Give the position of every Plasmodium parasite and every leukocyte.
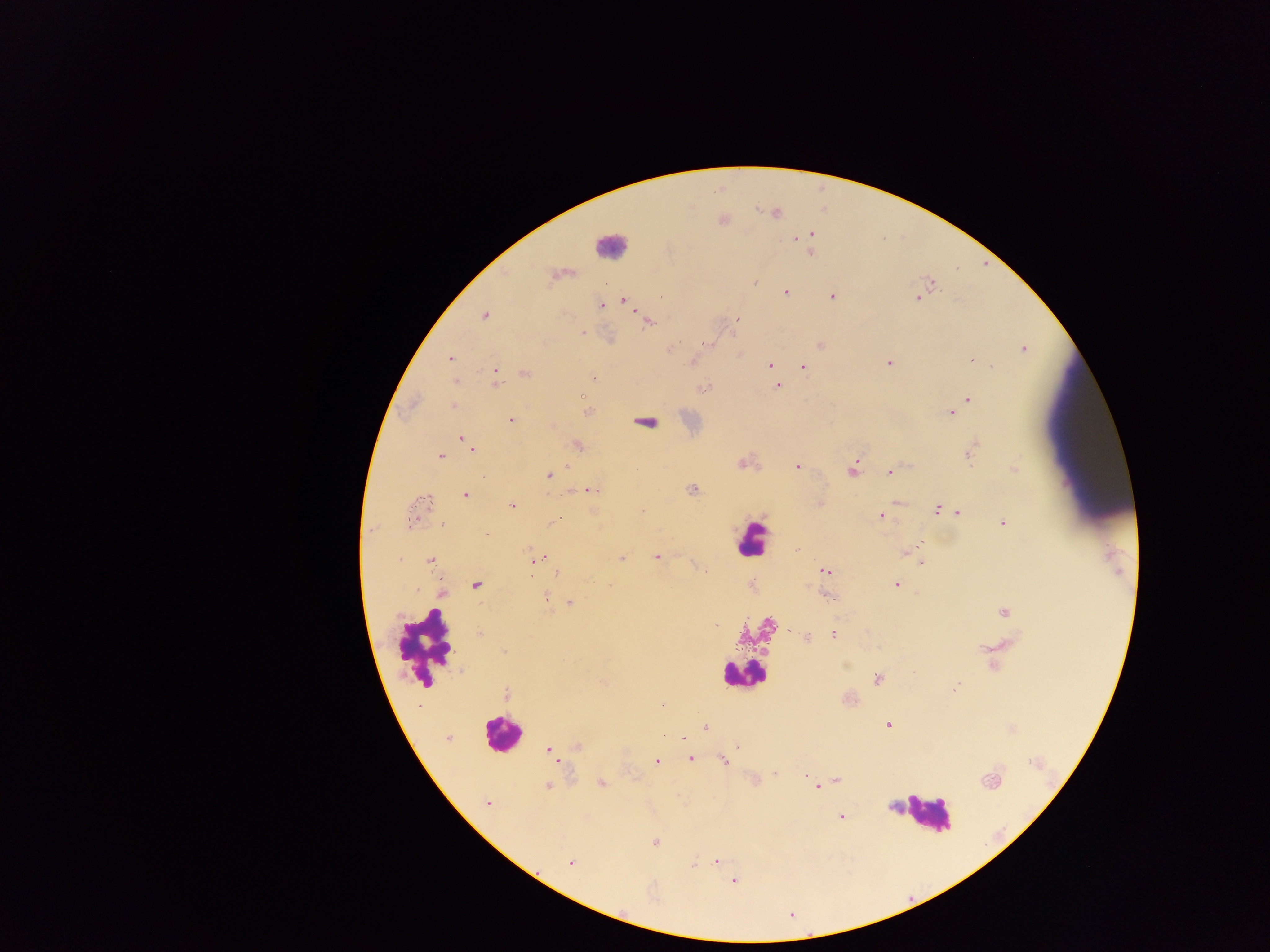

Approximate centers as {x, y} in pixels.
Plasmodium parasites: {775, 214}, {811, 235}, {795, 239}, {811, 252}, {931, 282}, {785, 292}, {832, 296}, {917, 298}, {623, 300}, {601, 305}, {484, 317}, {738, 319}, {647, 322}, {582, 332}, {706, 343}, {822, 345}, {669, 349}, {1024, 349}, {450, 358}, {972, 359}, {984, 362}, {888, 363}, {769, 365}, {803, 367}, {992, 367}, {525, 373}, {773, 373}, {496, 374}, {593, 379}, {455, 381}, {777, 386}, {704, 388}, {968, 399}, {453, 405}, {951, 413}, {510, 420}, {462, 438}, {468, 443}, {577, 445}, {472, 449}, {970, 453}, {440, 457}, {743, 463}, {796, 466}, {566, 467}, {1014, 468}, {636, 469}, {853, 469}, {554, 472}, {891, 473}, {548, 475}, {693, 489}, {591, 490}, {465, 495}, {424, 504}, {511, 505}, {937, 510}, {642, 511}, {958, 513}, {881, 515}, {444, 523}, {552, 523}, {1002, 523}, {485, 533}, {919, 547}, {796, 548}, {905, 553}, {656, 557}, {621, 558}, {537, 559}, {430, 561}, {921, 562}, {827, 571}, {556, 573}, {896, 584}, {475, 585}, {441, 593}, {546, 596}, {828, 596}, {570, 604}, {1004, 611}, {716, 625}, {834, 634}, {479, 635}, {807, 637}, {504, 652}, {877, 679}, {602, 682}, {957, 686}, {506, 694}, {662, 705}, {887, 725}, {706, 728}, {447, 738}, {683, 739}, {578, 746}, {738, 746}, {548, 749}, {690, 758}, {656, 761}, {723, 762}, {805, 775}, {837, 780}, {991, 781}, {601, 783}, {547, 787}, {817, 787}, {488, 803}, {842, 817}, {655, 842}, {570, 862}, {716, 862}, {693, 864}, {733, 881}.
Leukocytes: {608, 245}, {647, 422}, {750, 539}, {426, 646}, {741, 673}, {500, 733}, {926, 813}.

Thick blood film. Collected in Ghana. One field of view. Mobile-phone photograph taken through the microscope. Image is 1270×952 pixels.